State which parasite is depicted.
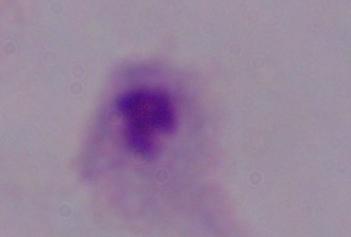
A trichomonad.

magnification = 1000x
modality = micrograph